Locate every blood parasite and identify its species.
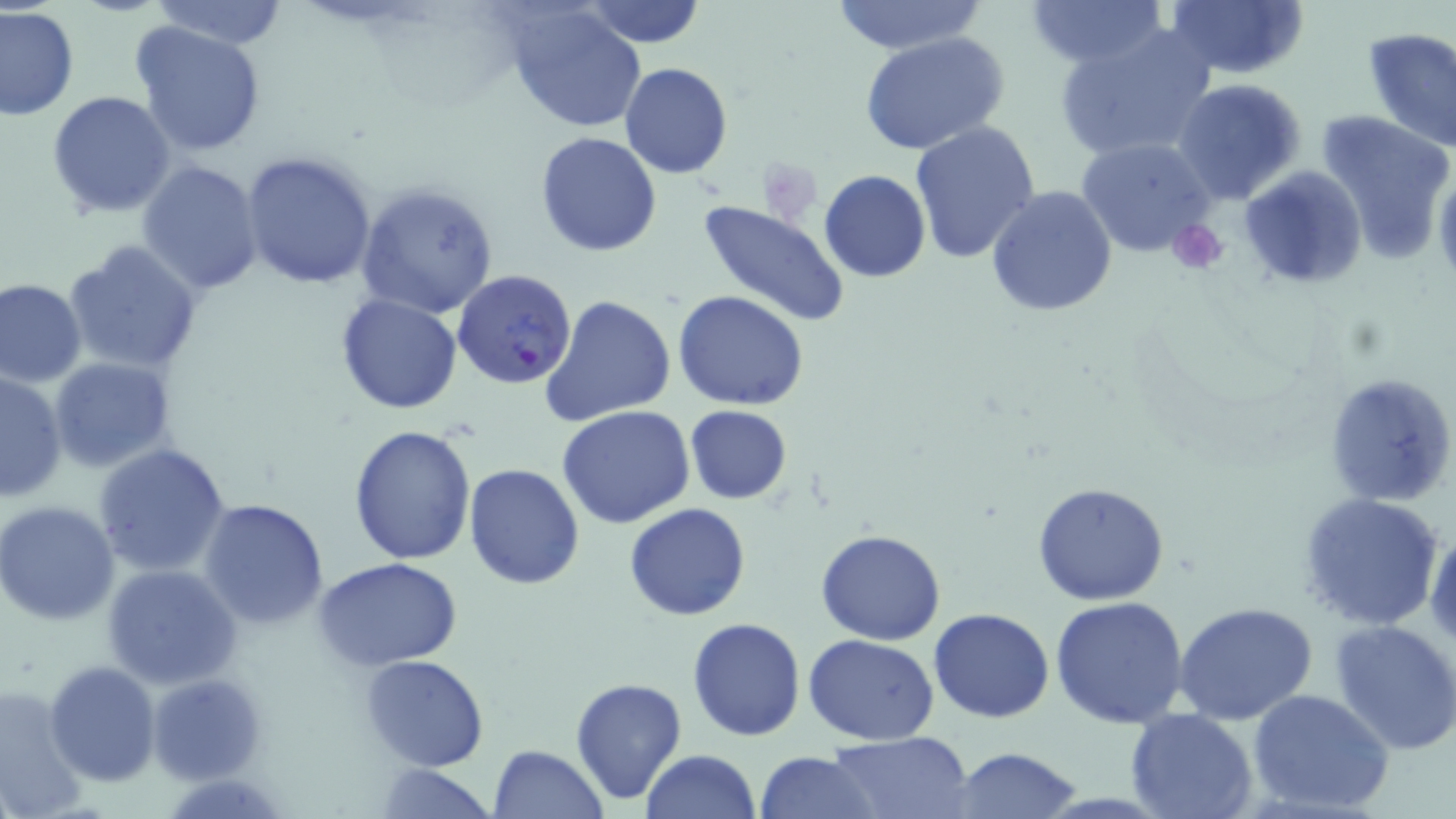
Approximate bounding boxes as (x1, y1, x2, y2) in pixels.
Plasmodium falciparum-infected red blood cells: (454, 269, 578, 389).
No Plasmodium ovale, Plasmodium malariae, Plasmodium vivax, Babesia divergens, or Trypanosoma brucei observed.

Summary:
  - Platelet locations: (758, 157, 822, 222), (1167, 219, 1230, 276)
  - Uninfected red blood cell locations: (150, 0, 291, 49), (1025, 0, 1170, 70), (1163, 0, 1311, 79), (583, 1, 708, 48), (827, 1, 987, 55), (0, 6, 79, 120), (505, 6, 648, 132), (132, 20, 267, 158), (1052, 23, 1218, 164), (1361, 27, 1456, 152), (859, 32, 1009, 154), (620, 62, 732, 178), (1171, 79, 1310, 206), (45, 89, 177, 219), (1316, 109, 1455, 264), (908, 121, 1041, 267), (536, 131, 662, 256), (1075, 136, 1218, 258), (241, 150, 381, 289), (137, 161, 264, 295), (1238, 164, 1369, 289), (818, 169, 931, 283), (356, 182, 498, 320), (986, 185, 1118, 318), (696, 200, 851, 330), (64, 238, 203, 374), (0, 278, 86, 387), (674, 291, 808, 409), (336, 292, 463, 414), (540, 295, 677, 426), (49, 358, 178, 474), (1, 371, 68, 502), (1322, 371, 1456, 509), (684, 405, 793, 504), (556, 406, 697, 530), (349, 424, 476, 565), (93, 443, 234, 578), (462, 462, 584, 589), (1030, 481, 1171, 605), (1297, 490, 1447, 632), (199, 497, 330, 629), (1, 500, 121, 625), (624, 503, 750, 620), (1426, 527, 1456, 655), (817, 528, 946, 644), (317, 557, 462, 671), (103, 565, 241, 689), (1049, 594, 1191, 728), (1173, 601, 1318, 726), (929, 608, 1055, 724), (686, 616, 808, 741), (1330, 620, 1456, 755), (804, 634, 939, 745), (362, 654, 490, 770), (44, 661, 161, 786), (148, 671, 266, 785), (570, 677, 688, 805), (0, 682, 88, 818), (1248, 687, 1394, 816), (1124, 709, 1260, 819), (825, 732, 975, 818), (487, 745, 608, 818), (950, 747, 1082, 818), (644, 748, 760, 819), (757, 750, 879, 818), (375, 764, 499, 818)
  - Slide-level diagnosis: Plasmodium falciparum
  - Stain: May-Grünwald-Giemsa
  - Preparation: thin blood smear
  - Magnification: 1000x
  - Modality: light microscopy
  - Image size: 1456×819 pixels
  - Field of view: one of a larger specimen